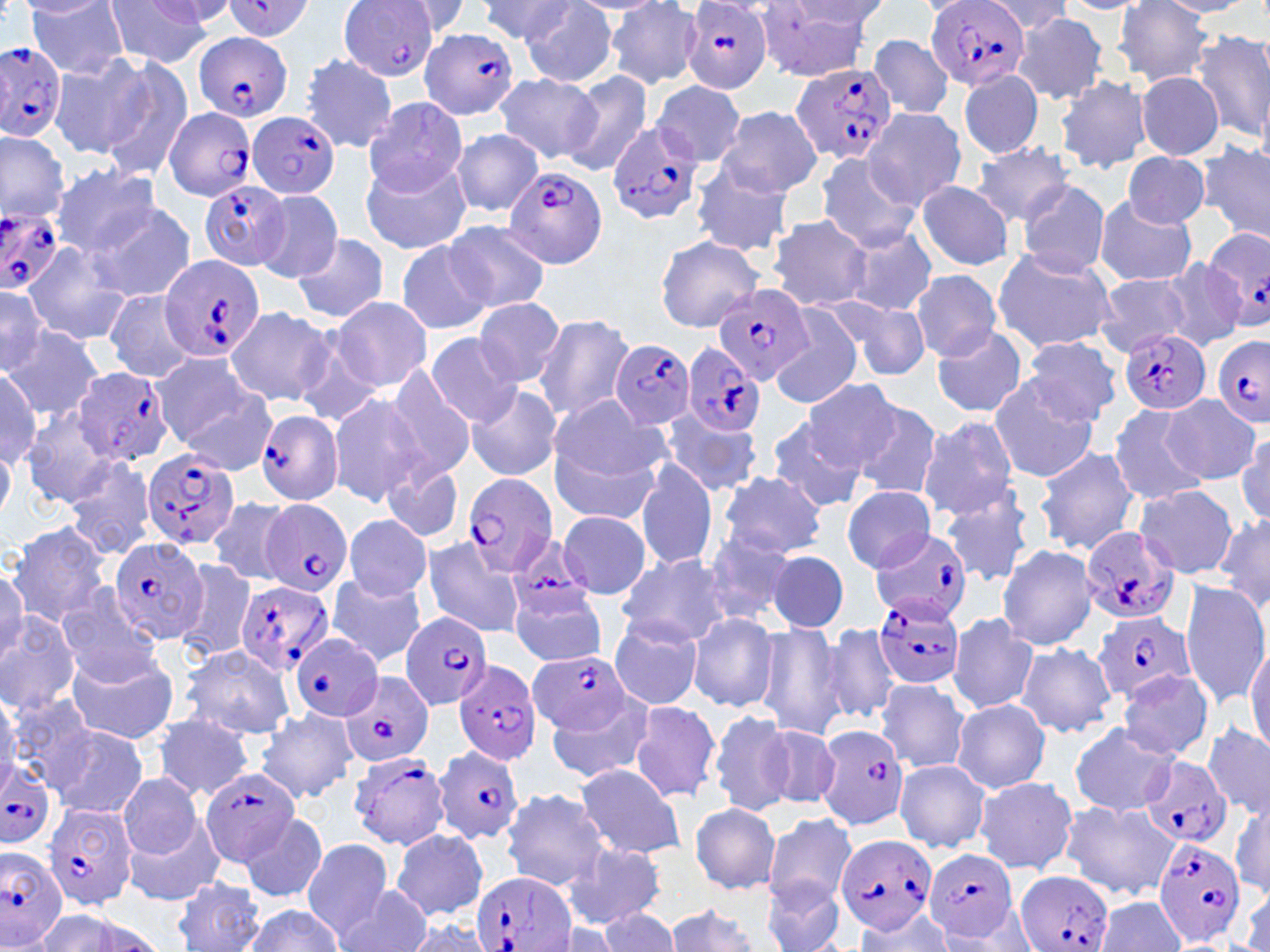
slide-level diagnosis = Plasmodium falciparum
stain = May-Grünwald-Giemsa
uninfected red blood cell locations = approximate bounding boxes as named x1/y1/x2/y2 corners in pixels: (x1=27, y1=0, x2=128, y2=79), (x1=978, y1=0, x2=1074, y2=34), (x1=103, y1=1, x2=213, y2=67), (x1=140, y1=1, x2=234, y2=28), (x1=392, y1=1, x2=474, y2=36), (x1=475, y1=1, x2=577, y2=41), (x1=565, y1=1, x2=668, y2=15), (x1=755, y1=1, x2=878, y2=84), (x1=1054, y1=1, x2=1152, y2=14), (x1=1152, y1=1, x2=1254, y2=16), (x1=21, y1=2, x2=115, y2=22), (x1=519, y1=3, x2=618, y2=87), (x1=605, y1=3, x2=703, y2=88), (x1=1114, y1=3, x2=1214, y2=85), (x1=1011, y1=13, x2=1110, y2=103), (x1=1192, y1=30, x2=1270, y2=141), (x1=867, y1=34, x2=955, y2=121), (x1=51, y1=54, x2=152, y2=155), (x1=299, y1=54, x2=400, y2=154), (x1=95, y1=57, x2=193, y2=178), (x1=960, y1=69, x2=1044, y2=159), (x1=563, y1=71, x2=654, y2=177), (x1=1137, y1=71, x2=1224, y2=161), (x1=494, y1=72, x2=603, y2=166), (x1=1053, y1=74, x2=1151, y2=175), (x1=652, y1=80, x2=749, y2=167), (x1=363, y1=95, x2=468, y2=197), (x1=715, y1=105, x2=823, y2=198), (x1=862, y1=109, x2=966, y2=210), (x1=450, y1=129, x2=544, y2=215), (x1=0, y1=132, x2=69, y2=225), (x1=1198, y1=141, x2=1270, y2=244), (x1=973, y1=143, x2=1076, y2=223), (x1=1121, y1=151, x2=1210, y2=229), (x1=813, y1=153, x2=923, y2=251), (x1=360, y1=156, x2=472, y2=255), (x1=51, y1=162, x2=162, y2=258), (x1=689, y1=163, x2=795, y2=258), (x1=914, y1=180, x2=1015, y2=271), (x1=1016, y1=180, x2=1110, y2=279), (x1=253, y1=189, x2=346, y2=283), (x1=1092, y1=195, x2=1198, y2=287), (x1=89, y1=205, x2=194, y2=302), (x1=768, y1=215, x2=871, y2=311), (x1=442, y1=220, x2=551, y2=317), (x1=844, y1=226, x2=938, y2=315), (x1=654, y1=234, x2=764, y2=332), (x1=291, y1=235, x2=390, y2=323), (x1=392, y1=239, x2=493, y2=336), (x1=21, y1=241, x2=133, y2=346), (x1=994, y1=247, x2=1119, y2=353), (x1=1153, y1=260, x2=1245, y2=351), (x1=911, y1=269, x2=1002, y2=361), (x1=1094, y1=273, x2=1192, y2=358), (x1=0, y1=277, x2=51, y2=375), (x1=103, y1=290, x2=197, y2=382), (x1=329, y1=297, x2=432, y2=392), (x1=473, y1=297, x2=564, y2=387), (x1=834, y1=297, x2=929, y2=381), (x1=224, y1=307, x2=334, y2=407), (x1=770, y1=310, x2=862, y2=407), (x1=534, y1=314, x2=635, y2=422), (x1=931, y1=326, x2=1028, y2=419), (x1=6, y1=328, x2=102, y2=420), (x1=424, y1=332, x2=521, y2=427), (x1=1023, y1=336, x2=1122, y2=425), (x1=150, y1=352, x2=263, y2=450), (x1=381, y1=364, x2=476, y2=479), (x1=0, y1=370, x2=41, y2=468), (x1=987, y1=376, x2=1098, y2=483), (x1=799, y1=378, x2=902, y2=471), (x1=173, y1=381, x2=280, y2=475), (x1=465, y1=384, x2=563, y2=482), (x1=327, y1=393, x2=424, y2=506), (x1=548, y1=394, x2=669, y2=488), (x1=1162, y1=396, x2=1258, y2=485), (x1=848, y1=400, x2=944, y2=503), (x1=1106, y1=402, x2=1211, y2=506), (x1=19, y1=410, x2=123, y2=506), (x1=657, y1=410, x2=763, y2=497), (x1=917, y1=416, x2=1020, y2=520), (x1=765, y1=417, x2=870, y2=512), (x1=549, y1=430, x2=664, y2=526), (x1=1236, y1=430, x2=1270, y2=529), (x1=1035, y1=445, x2=1142, y2=555), (x1=0, y1=446, x2=15, y2=524), (x1=62, y1=456, x2=158, y2=561), (x1=634, y1=460, x2=718, y2=572), (x1=381, y1=461, x2=465, y2=544), (x1=716, y1=472, x2=827, y2=558), (x1=1135, y1=484, x2=1238, y2=578), (x1=843, y1=486, x2=934, y2=572), (x1=939, y1=495, x2=1034, y2=589), (x1=209, y1=499, x2=292, y2=585), (x1=558, y1=510, x2=651, y2=600), (x1=342, y1=513, x2=432, y2=603), (x1=1214, y1=514, x2=1270, y2=616), (x1=7, y1=522, x2=110, y2=628), (x1=700, y1=529, x2=802, y2=627), (x1=422, y1=538, x2=524, y2=638), (x1=996, y1=542, x2=1099, y2=650), (x1=768, y1=550, x2=848, y2=633), (x1=615, y1=552, x2=732, y2=646), (x1=172, y1=562, x2=258, y2=660), (x1=0, y1=566, x2=27, y2=657), (x1=327, y1=575, x2=425, y2=666), (x1=1180, y1=580, x2=1269, y2=708), (x1=53, y1=584, x2=160, y2=682), (x1=509, y1=586, x2=608, y2=665), (x1=0, y1=611, x2=82, y2=715), (x1=687, y1=613, x2=779, y2=713), (x1=948, y1=614, x2=1039, y2=714), (x1=609, y1=617, x2=704, y2=710), (x1=819, y1=622, x2=903, y2=726), (x1=756, y1=624, x2=849, y2=741), (x1=1245, y1=640, x2=1270, y2=753), (x1=1015, y1=642, x2=1117, y2=738), (x1=43, y1=644, x2=159, y2=811), (x1=179, y1=644, x2=295, y2=739), (x1=63, y1=646, x2=179, y2=745), (x1=1119, y1=669, x2=1213, y2=759), (x1=875, y1=678, x2=971, y2=775), (x1=0, y1=690, x2=20, y2=789), (x1=5, y1=693, x2=100, y2=792), (x1=545, y1=695, x2=653, y2=784), (x1=951, y1=699, x2=1050, y2=794), (x1=629, y1=700, x2=723, y2=803), (x1=256, y1=708, x2=358, y2=802), (x1=708, y1=710, x2=796, y2=816), (x1=151, y1=713, x2=256, y2=800), (x1=756, y1=722, x2=844, y2=813), (x1=1067, y1=723, x2=1177, y2=816), (x1=1203, y1=724, x2=1268, y2=816), (x1=50, y1=725, x2=149, y2=819), (x1=894, y1=760, x2=989, y2=852), (x1=576, y1=763, x2=686, y2=861), (x1=532, y1=768, x2=672, y2=914), (x1=120, y1=775, x2=201, y2=858), (x1=973, y1=777, x2=1078, y2=874), (x1=500, y1=789, x2=612, y2=891), (x1=1231, y1=795, x2=1270, y2=897), (x1=1060, y1=800, x2=1179, y2=900), (x1=690, y1=803, x2=780, y2=894), (x1=241, y1=813, x2=328, y2=902), (x1=125, y1=815, x2=223, y2=907), (x1=763, y1=815, x2=857, y2=907), (x1=393, y1=828, x2=487, y2=920), (x1=301, y1=838, x2=394, y2=941), (x1=561, y1=842, x2=666, y2=929), (x1=174, y1=877, x2=264, y2=951), (x1=763, y1=878, x2=847, y2=952), (x1=342, y1=884, x2=433, y2=952), (x1=1095, y1=896, x2=1184, y2=951), (x1=662, y1=904, x2=762, y2=952), (x1=242, y1=906, x2=345, y2=951), (x1=30, y1=908, x2=160, y2=952), (x1=598, y1=909, x2=680, y2=951), (x1=848, y1=909, x2=954, y2=950), (x1=400, y1=914, x2=495, y2=952)
preparation = thin blood film
field of view = one of a larger specimen
Plasmodium falciparum-infected red blood cell locations = approximate bounding boxes as named x1/y1/x2/y2 corners in pixels: (x1=221, y1=0, x2=317, y2=41), (x1=342, y1=0, x2=438, y2=83), (x1=927, y1=0, x2=1029, y2=93), (x1=680, y1=2, x2=773, y2=94), (x1=418, y1=28, x2=519, y2=120), (x1=192, y1=31, x2=294, y2=122), (x1=0, y1=39, x2=67, y2=142), (x1=790, y1=62, x2=898, y2=167), (x1=162, y1=106, x2=257, y2=201), (x1=248, y1=111, x2=341, y2=198), (x1=607, y1=119, x2=702, y2=226), (x1=502, y1=164, x2=610, y2=269), (x1=198, y1=182, x2=290, y2=270), (x1=0, y1=206, x2=66, y2=292), (x1=1202, y1=224, x2=1270, y2=331), (x1=156, y1=252, x2=265, y2=362), (x1=713, y1=284, x2=813, y2=384), (x1=1121, y1=327, x2=1211, y2=416), (x1=1213, y1=336, x2=1270, y2=428), (x1=610, y1=339, x2=696, y2=428), (x1=679, y1=343, x2=765, y2=437), (x1=73, y1=368, x2=173, y2=466), (x1=255, y1=409, x2=343, y2=504), (x1=140, y1=449, x2=239, y2=551), (x1=462, y1=472, x2=557, y2=576), (x1=261, y1=499, x2=354, y2=597), (x1=1080, y1=526, x2=1179, y2=623), (x1=871, y1=530, x2=974, y2=625), (x1=108, y1=537, x2=210, y2=644), (x1=505, y1=539, x2=599, y2=620), (x1=234, y1=580, x2=333, y2=677), (x1=872, y1=594, x2=965, y2=689), (x1=1092, y1=611, x2=1196, y2=703), (x1=399, y1=612, x2=493, y2=710), (x1=290, y1=633, x2=381, y2=722), (x1=532, y1=650, x2=631, y2=738), (x1=453, y1=658, x2=544, y2=764), (x1=341, y1=671, x2=434, y2=768), (x1=817, y1=728, x2=912, y2=835), (x1=435, y1=746, x2=525, y2=843), (x1=348, y1=752, x2=451, y2=850), (x1=1139, y1=757, x2=1231, y2=849), (x1=0, y1=759, x2=57, y2=844), (x1=200, y1=766, x2=302, y2=868), (x1=43, y1=801, x2=137, y2=910), (x1=835, y1=833, x2=936, y2=935), (x1=1153, y1=839, x2=1243, y2=946), (x1=0, y1=846, x2=69, y2=948), (x1=924, y1=849, x2=1021, y2=943), (x1=1017, y1=870, x2=1114, y2=952), (x1=473, y1=872, x2=578, y2=952)
modality = light microscopy
magnification = 1000x
image size = 1270×952 pixels